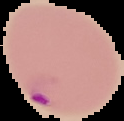 The area outside the segmented cell region is set to black. From a thin blood smear. Image is 124×121 pixels. Malaria status: parasitized.